Locate every Plasmodium parasite.
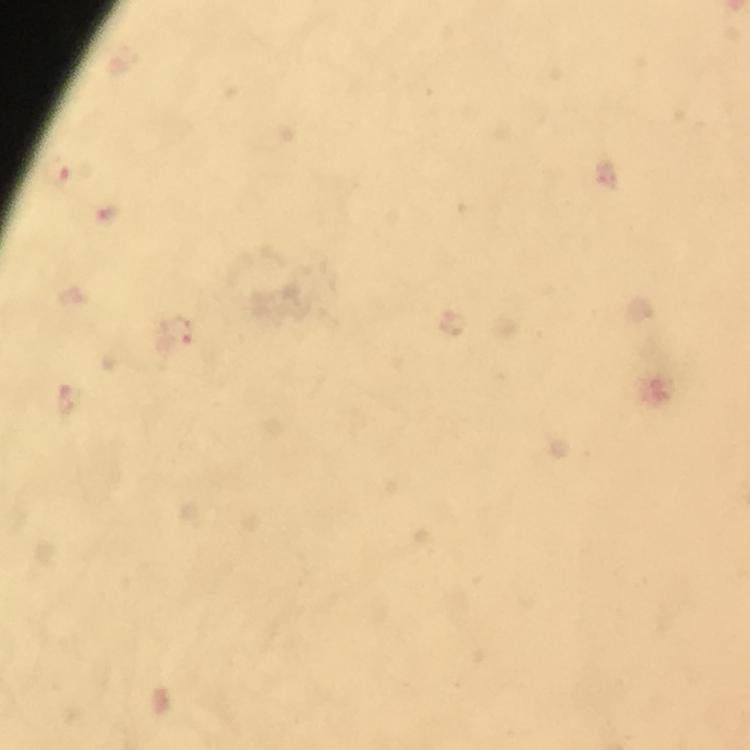
Approximate centers as (x, y) in pixels.
Plasmodium parasites: (56, 172), (177, 329).

Summary:
  - Magnification: 100x
  - Cropped from: a single field of view
  - Stain: Giemsa
  - Context: from a malaria diagnostic workup
  - Capture: smartphone camera through the microscope
  - Image size: 750×750 pixels
  - Preparation: thick blood film
  - Immersion oil: applied